Assess this cell for malaria.
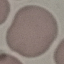

Uninfected.

stain: Giemsa
capture: smartphone camera at the microscope eyepiece
preparation: thin smear
image_type: cell patch, automatically extracted from a larger field of view and resized to 64 × 64 pixels